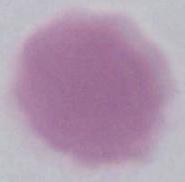

magnification = 1000x
identification = red blood cell
modality = photomicrograph